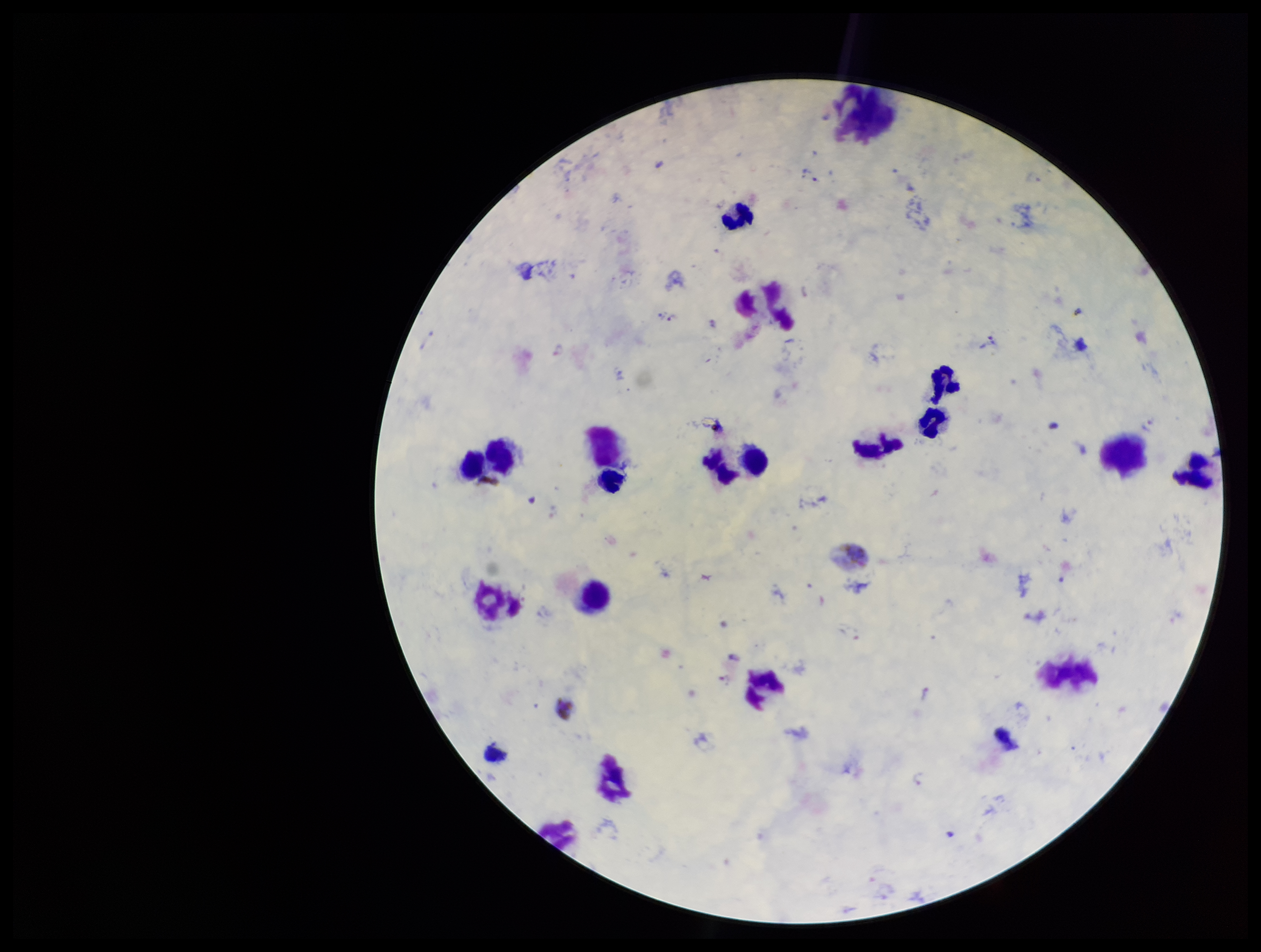 Preparation: thick blood smear. Plasmodium parasites: identified. Single field of view. Stained with Giemsa. Patient malaria status: infected. Species reported for this patient: Plasmodium vivax. Leukocyte count: 12. Image is 1261×952 pixels. Smartphone photograph taken through the eyepiece of a microscope. Parasite count: 3.